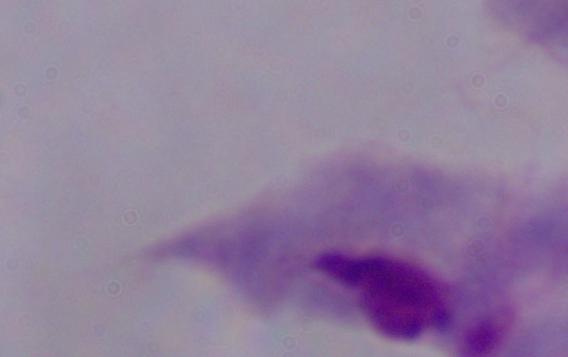

modality = micrograph
identification = trichomonad
magnification = 1000x